Name the parasite shown.
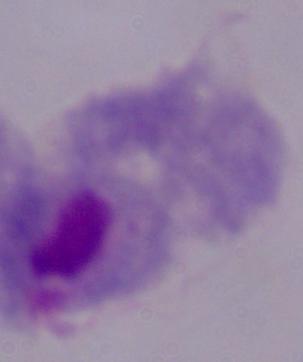
A trichomonad.

magnification = 1000x
modality = micrograph